Describe the morphology of the red blood cells.
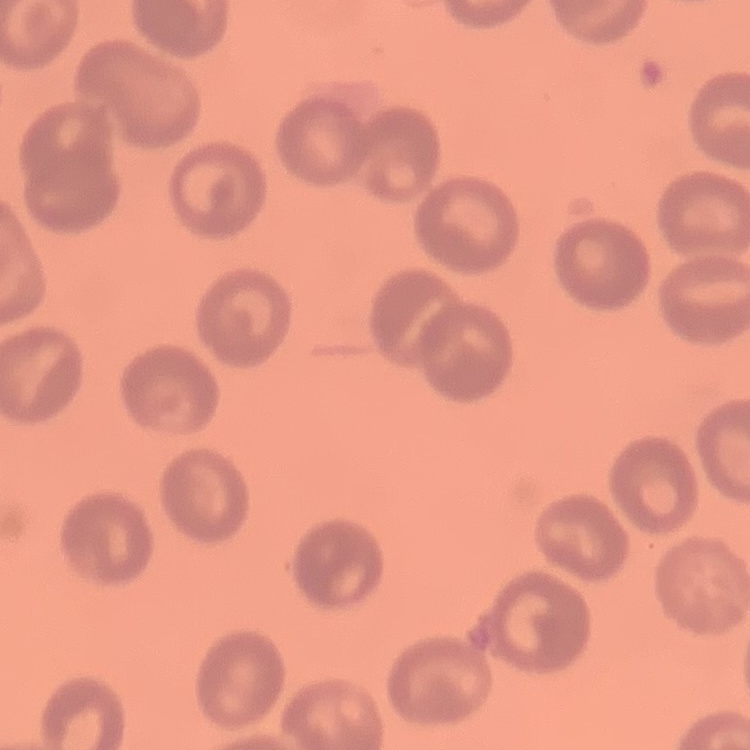
No rouleaux formation.

image type = square crop of a larger photomicrograph
stain = Field's or Giemsa
preparation = thin peripheral smear